Give the extent of all uninfected red blood cells.
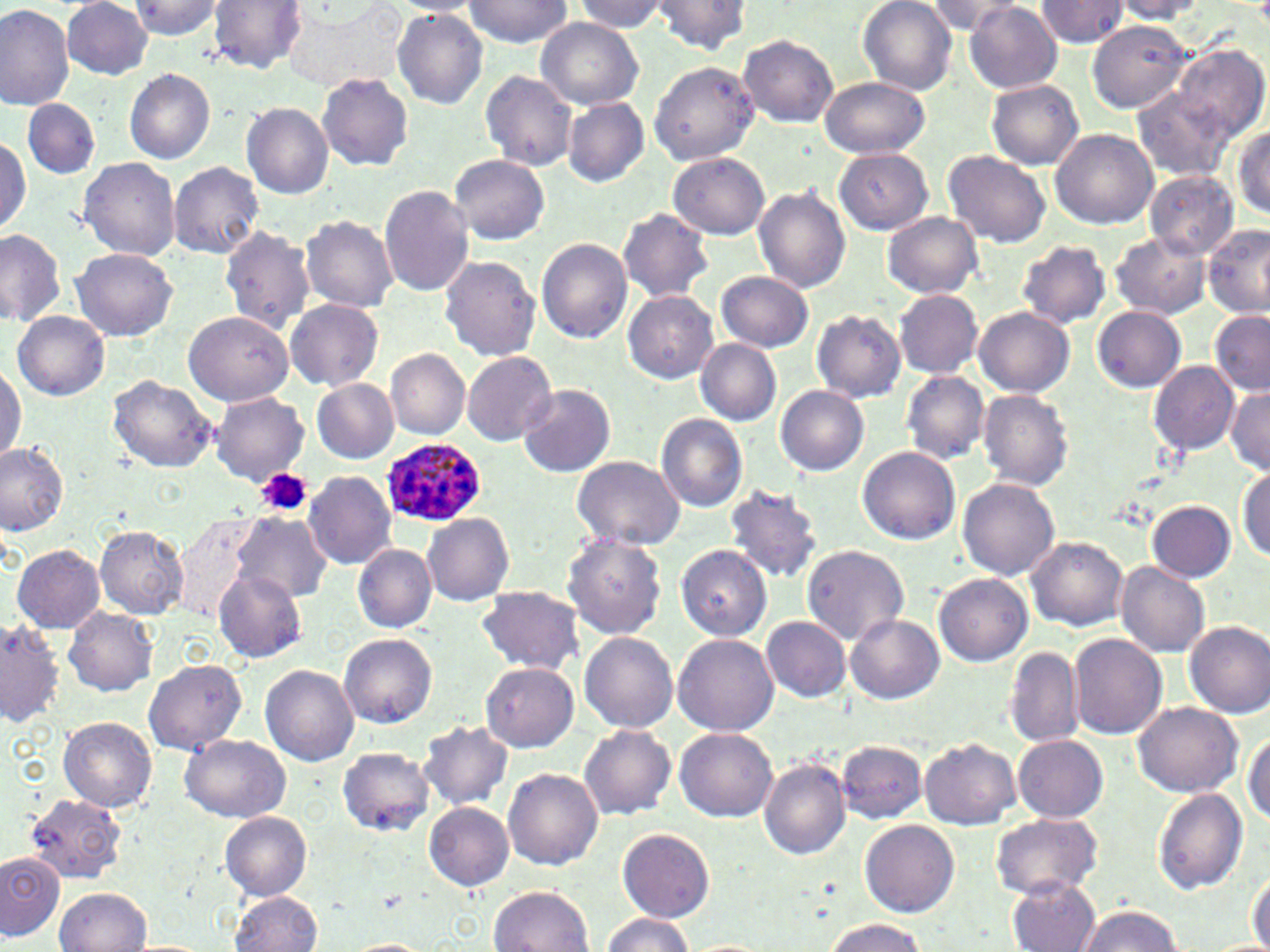
Approximate bounding boxes as (x1, y1, x2, y2) in pixels.
Uninfected red blood cells: (61, 0, 153, 79), (208, 0, 307, 74), (288, 0, 405, 95), (463, 0, 572, 47), (858, 0, 957, 94), (925, 0, 1021, 36), (128, 1, 224, 39), (387, 1, 482, 15), (574, 1, 668, 33), (648, 1, 754, 54), (1037, 1, 1129, 47), (1110, 1, 1208, 22), (0, 3, 76, 111), (965, 4, 1062, 93), (392, 9, 487, 108), (536, 19, 644, 109), (1087, 20, 1194, 114), (738, 34, 838, 128), (1173, 46, 1267, 141), (649, 61, 759, 167), (124, 68, 216, 163), (481, 70, 578, 170), (317, 73, 414, 171), (819, 77, 929, 159), (986, 79, 1085, 169), (1129, 87, 1235, 182), (563, 97, 649, 187), (23, 98, 99, 179), (242, 102, 334, 199), (1230, 123, 1270, 219), (1050, 128, 1160, 230), (0, 135, 30, 234), (834, 148, 933, 234), (943, 149, 1050, 248), (668, 152, 771, 240), (451, 153, 550, 244), (78, 157, 182, 262), (168, 161, 264, 259), (1145, 170, 1239, 260), (378, 186, 475, 297), (753, 187, 850, 294), (615, 208, 716, 302), (883, 211, 983, 297), (300, 215, 399, 311), (1203, 224, 1270, 317), (218, 225, 316, 333), (0, 229, 67, 325), (1109, 233, 1212, 319), (536, 237, 632, 343), (1016, 241, 1112, 328), (70, 247, 178, 341), (439, 255, 541, 362), (715, 271, 814, 353), (894, 290, 983, 377), (623, 291, 719, 384), (284, 299, 384, 390), (1092, 307, 1185, 392), (974, 308, 1074, 397), (183, 310, 293, 405), (13, 311, 109, 400), (811, 311, 906, 402), (1208, 311, 1270, 396), (696, 339, 781, 425), (386, 348, 470, 439), (461, 352, 556, 444), (1149, 361, 1240, 455), (0, 365, 23, 464), (901, 370, 990, 463), (108, 376, 218, 473), (311, 379, 399, 462), (517, 383, 616, 478), (775, 385, 868, 476), (1225, 387, 1270, 475), (977, 390, 1074, 489), (210, 392, 309, 483), (656, 414, 750, 513), (0, 443, 69, 535), (859, 445, 961, 545), (571, 455, 684, 549), (1237, 469, 1270, 563), (303, 470, 396, 568), (957, 479, 1059, 580), (724, 483, 825, 582), (1148, 500, 1236, 581), (232, 513, 331, 605), (422, 513, 514, 606), (177, 515, 258, 625), (94, 526, 188, 618), (563, 535, 667, 641), (1027, 535, 1129, 630), (353, 544, 436, 632), (675, 544, 771, 642), (801, 544, 910, 645), (12, 545, 104, 633), (1116, 561, 1211, 658), (215, 567, 307, 662), (933, 573, 1032, 667), (476, 585, 584, 673), (64, 608, 158, 696), (847, 614, 944, 703), (760, 617, 849, 702), (0, 620, 64, 728), (1185, 620, 1270, 717), (339, 631, 437, 728), (580, 631, 677, 734), (672, 634, 779, 738), (1068, 634, 1168, 741), (1005, 646, 1085, 748), (142, 658, 249, 755), (482, 662, 578, 751), (261, 664, 358, 768), (1132, 701, 1242, 798), (59, 716, 157, 812), (418, 721, 513, 810), (580, 725, 675, 819), (676, 728, 778, 821), (1245, 729, 1270, 828), (180, 734, 290, 822), (1014, 736, 1108, 822), (919, 737, 1021, 829), (836, 740, 927, 824), (338, 747, 435, 836), (758, 759, 850, 860), (504, 769, 602, 870), (1153, 788, 1247, 895), (22, 792, 128, 884), (424, 803, 514, 890), (219, 811, 313, 899), (990, 812, 1104, 898), (861, 819, 959, 918), (619, 828, 714, 923), (0, 852, 66, 941), (1248, 869, 1270, 952), (1006, 879, 1101, 952), (490, 886, 594, 952), (53, 888, 152, 952), (230, 891, 324, 951), (1076, 905, 1182, 952), (601, 913, 695, 951), (823, 918, 925, 952), (346, 938, 432, 952).

slide-level diagnosis = Plasmodium ovale
preparation = thin blood smear
field of view = one of a larger specimen
platelet locations = approximate bounding boxes as (x1, y1, x2, y2) in pixels: (256, 467, 313, 517)
image size = 1270×952 pixels
Plasmodium ovale-infected red blood cell locations = approximate bounding boxes as (x1, y1, x2, y2) in pixels: (381, 437, 488, 527)
magnification = 1000x
modality = optical microscopy
stain = May-Grünwald-Giemsa